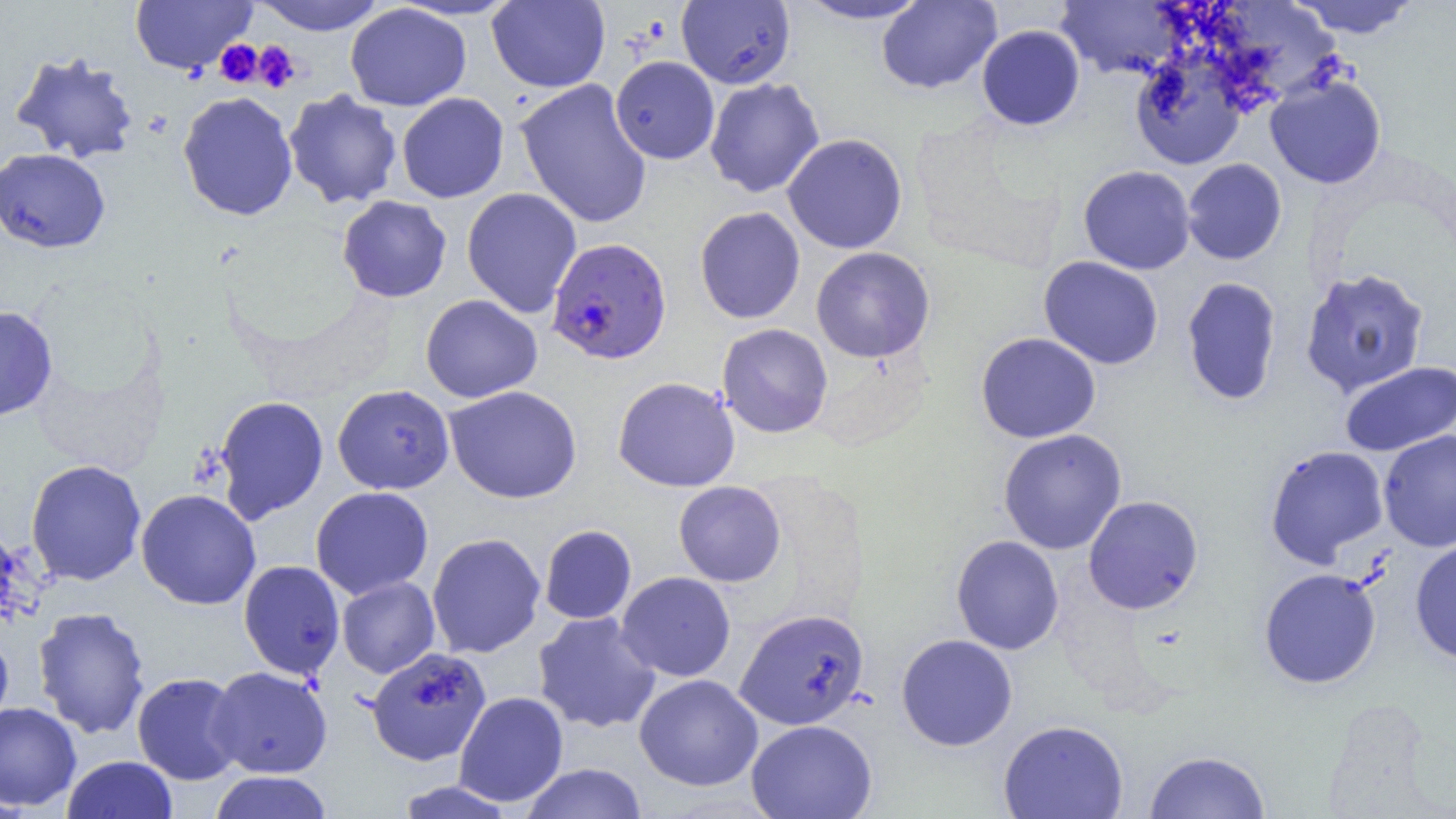 Approximate bounding boxes as [x1, y1, x2, y2] in pixels. Platelet locations: [215, 39, 263, 87], [252, 41, 301, 93]. Uninfected red blood cell locations: [129, 0, 257, 75], [250, 0, 387, 35], [793, 0, 932, 25], [1289, 0, 1421, 38], [487, 1, 610, 93], [677, 1, 796, 89], [876, 1, 1002, 94], [1054, 1, 1188, 79], [345, 3, 471, 111], [977, 25, 1085, 130], [10, 50, 141, 165], [1130, 51, 1249, 170], [610, 56, 720, 164], [1265, 73, 1387, 189], [705, 77, 825, 198], [515, 78, 653, 229], [283, 89, 402, 210], [177, 91, 298, 221], [396, 92, 509, 203], [782, 133, 908, 254], [0, 148, 111, 253], [1182, 158, 1287, 265], [1078, 165, 1196, 274], [462, 187, 582, 318], [336, 195, 452, 303], [694, 207, 805, 324], [810, 246, 935, 363], [1038, 256, 1164, 370], [1299, 267, 1430, 398], [1181, 276, 1282, 406], [420, 294, 542, 403], [0, 305, 59, 421], [716, 323, 833, 439], [975, 332, 1101, 443], [1339, 360, 1456, 457], [612, 376, 741, 492], [332, 384, 455, 495], [444, 385, 582, 504], [213, 395, 329, 523], [997, 428, 1127, 555], [1378, 430, 1456, 552], [1264, 444, 1389, 567], [25, 459, 147, 586], [673, 481, 786, 587], [310, 486, 434, 600], [135, 489, 261, 610], [1083, 494, 1204, 615], [539, 524, 637, 624], [426, 532, 546, 658], [950, 534, 1064, 655], [1409, 538, 1456, 666], [238, 560, 345, 680], [1258, 568, 1382, 689], [616, 571, 736, 681], [336, 576, 440, 678], [32, 606, 150, 739], [735, 608, 870, 730], [532, 611, 662, 735], [0, 628, 14, 733], [896, 633, 1018, 751], [366, 647, 492, 766], [207, 666, 333, 778], [132, 672, 244, 785], [634, 674, 763, 791], [453, 691, 568, 807], [0, 701, 82, 811], [746, 719, 877, 819], [998, 719, 1128, 818], [1144, 749, 1270, 819], [62, 755, 178, 819], [521, 762, 647, 819], [209, 771, 333, 819]. Plasmodium falciparum-infected red blood cell locations: [546, 237, 672, 365]. Slide-level diagnosis: Plasmodium falciparum. One field of a larger specimen. Image is 1456×819 pixels. Optical microscopy. Thin blood smear. 1000x magnification.